Assess the morphology of the erythrocytes.
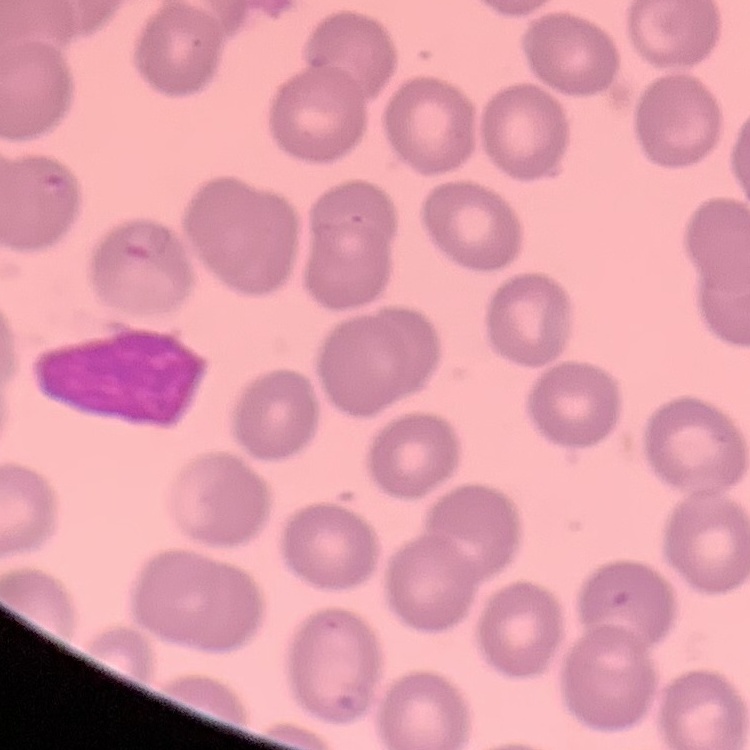
They show no rouleaux formation.

Square crop of a larger photomicrograph. Thin peripheral smear. Stained with either Field's or Giemsa.